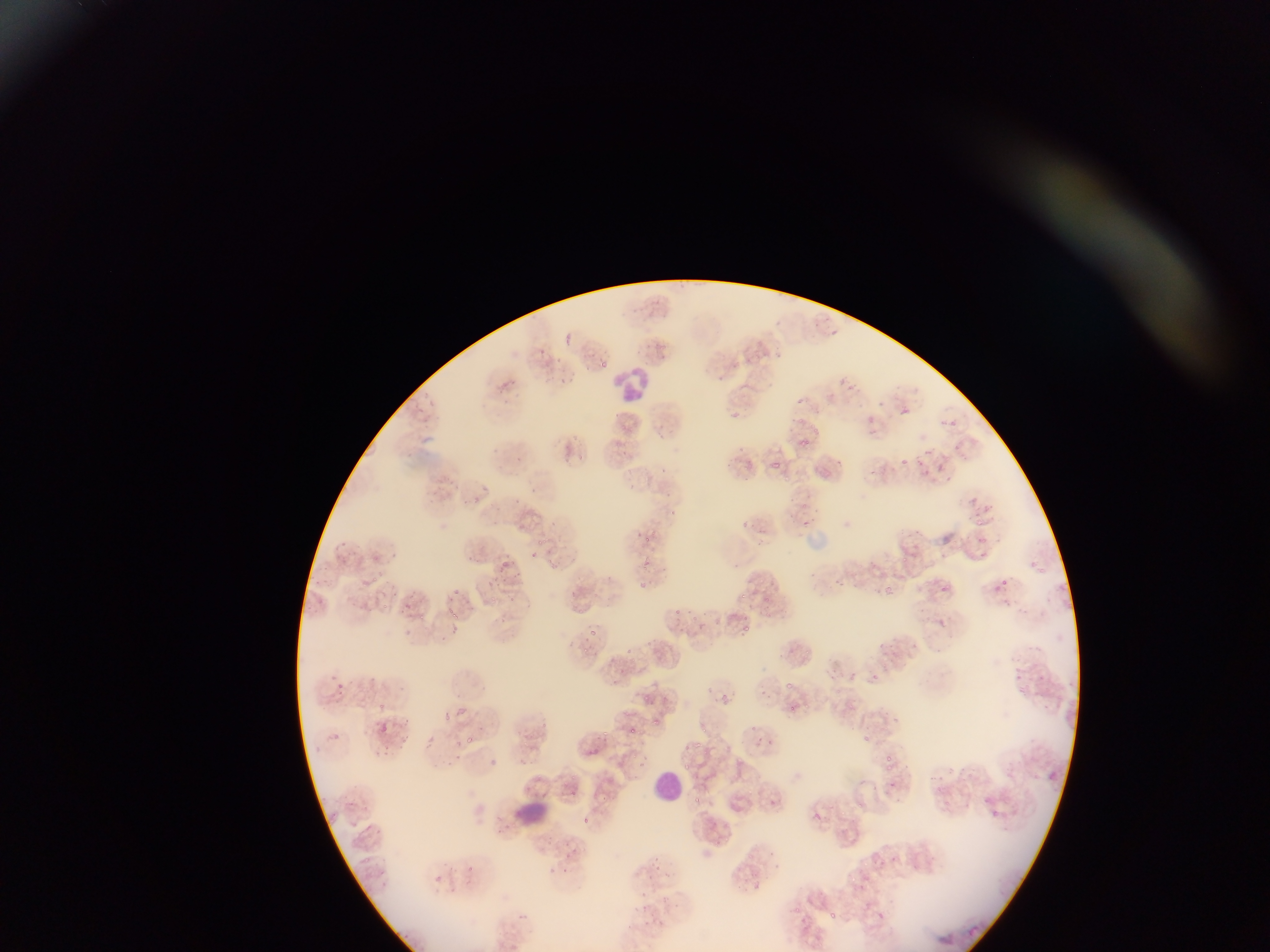

Approximate bounding boxes as {left, top, right, bottom} in pixels.
Summary:
  - Leukocyte locations: {616, 367, 650, 402}, {652, 767, 679, 801}, {508, 795, 554, 831}
  - Malaria parasite locations: {566, 331, 573, 350}, {537, 349, 547, 355}, {773, 351, 782, 361}, {748, 356, 755, 365}, {600, 360, 608, 370}, {733, 361, 739, 369}, {564, 377, 581, 396}, {797, 396, 810, 404}, {430, 397, 439, 406}, {901, 407, 912, 414}, {732, 410, 741, 421}, {868, 415, 878, 425}, {950, 417, 956, 429}, {812, 424, 820, 434}, {659, 434, 669, 442}, {802, 434, 811, 451}, {953, 445, 959, 453}, {924, 449, 935, 456}, {944, 453, 952, 462}, {579, 454, 585, 462}, {516, 455, 523, 463}, {914, 455, 925, 466}, {835, 457, 844, 464}, {902, 457, 911, 467}, {771, 460, 780, 468}, {746, 461, 756, 473}, {939, 462, 948, 473}, {661, 467, 668, 475}, {870, 468, 878, 476}, {924, 468, 930, 476}, {784, 475, 794, 483}, {628, 481, 637, 491}, {666, 492, 675, 500}, {467, 494, 483, 509}, {799, 503, 809, 511}, {983, 504, 998, 514}, {977, 518, 986, 526}, {739, 520, 752, 529}, {801, 520, 811, 526}, {330, 533, 352, 551}, {979, 536, 991, 545}, {539, 537, 552, 549}, {754, 541, 768, 550}, {940, 552, 948, 560}, {979, 552, 990, 557}, {547, 556, 554, 566}, {902, 556, 910, 564}, {497, 559, 524, 578}, {732, 563, 741, 570}, {640, 564, 655, 573}, {663, 566, 670, 575}, {1040, 566, 1050, 581}, {636, 577, 648, 591}, {1000, 578, 1009, 587}, {833, 579, 845, 586}, {994, 582, 1004, 594}, {756, 583, 766, 587}, {449, 584, 462, 597}, {938, 585, 949, 595}, {885, 586, 896, 595}, {592, 591, 601, 601}, {737, 593, 750, 600}, {765, 595, 771, 603}, {489, 596, 497, 608}, {1001, 597, 1014, 607}, {399, 600, 411, 614}, {382, 602, 392, 612}, {447, 606, 458, 618}, {578, 607, 584, 615}, {675, 608, 683, 618}, {418, 613, 428, 622}, {938, 617, 946, 626}, {407, 624, 412, 639}, {743, 624, 752, 633}, {588, 627, 597, 637}, {913, 641, 921, 652}, {583, 647, 588, 655}, {626, 647, 633, 656}, {893, 652, 901, 659}, {849, 667, 859, 681}, {328, 668, 347, 695}, {1015, 674, 1022, 683}, {785, 682, 798, 692}, {760, 687, 774, 703}, {721, 693, 730, 704}, {378, 700, 386, 715}, {1045, 701, 1053, 711}, {804, 702, 811, 711}, {789, 704, 793, 713}, {879, 705, 889, 717}, {442, 712, 451, 722}, {894, 717, 902, 725}, {653, 718, 661, 723}, {749, 725, 760, 734}, {702, 727, 711, 735}, {600, 728, 610, 740}, {757, 735, 765, 742}, {863, 735, 871, 743}, {401, 736, 411, 747}, {463, 736, 474, 743}, {768, 737, 775, 748}, {383, 742, 394, 761}, {693, 742, 703, 752}, {632, 753, 638, 761}, {882, 755, 893, 763}, {736, 757, 744, 764}, {683, 763, 692, 770}, {887, 764, 894, 772}, {948, 766, 955, 777}, {956, 767, 968, 776}, {535, 773, 545, 780}, {931, 775, 938, 783}, {891, 778, 896, 792}, {747, 786, 756, 799}, {945, 799, 953, 808}, {856, 803, 866, 808}, {990, 809, 998, 818}, {841, 810, 853, 823}, {813, 811, 822, 821}, {583, 816, 592, 830}, {546, 837, 555, 846}, {563, 842, 575, 851}, {746, 850, 754, 861}, {770, 850, 777, 859}, {564, 853, 573, 860}, {886, 854, 896, 864}, {651, 855, 660, 862}, {655, 865, 664, 870}, {562, 867, 573, 875}, {849, 876, 859, 884}, {752, 879, 761, 890}, {661, 893, 669, 905}, {639, 903, 648, 914}, {794, 906, 801, 915}, {878, 909, 887, 923}, {830, 910, 837, 919}, {644, 920, 654, 928}, {654, 920, 664, 928} | approximate {x, y} pixel centers of objects too small to bound: {834, 331}, {721, 378}, {841, 378}, {801, 420}, {946, 423}, {625, 452}, {631, 473}, {672, 513}, {653, 532}, {648, 539}, {1033, 564}, {375, 579}, {768, 613}, {706, 614}, {747, 620}, {881, 645}, {808, 651}, {874, 676}, {1040, 677}, {647, 696}, {633, 731}, {756, 744}, {685, 746}, {574, 777}, {938, 788}, {573, 792}, {699, 800}, {727, 838}, {776, 866}
  - Field of view: single
  - Preparation: thin blood film
  - Image size: 1270×952 pixels
  - Capture: mobile-phone photograph through a microscope
  - Country: Ghana